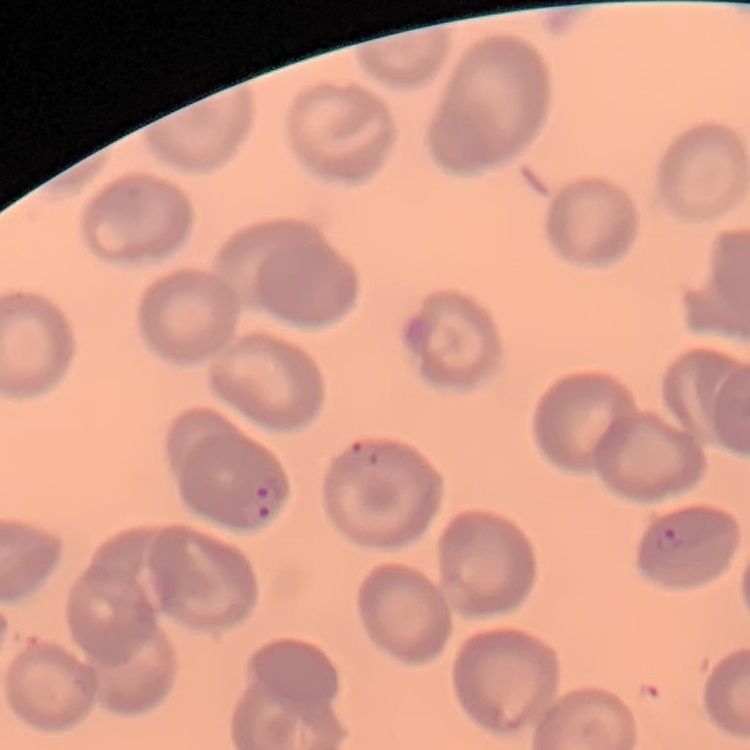
red_blood_cell_morphology: no rouleaux formation
image_type: one tile cut from a larger photomicrograph
preparation: thin blood film
stain: Field's or Giemsa